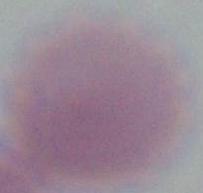
magnification = 1000x
identification = erythrocyte
modality = photomicrograph